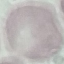
malaria_status: uninfected
capture: smartphone through the microscope eyepiece
preparation: thin smear
image_type: automatically extracted cell patch, resized to 64 × 64 pixels
stain: Giemsa